Assess this cell for malaria.
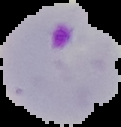
It is parasitized.

Summary:
  - Image type: segmented cell region with the area outside set to black
  - Image size: 121×127 pixels
  - Preparation: thin blood smear